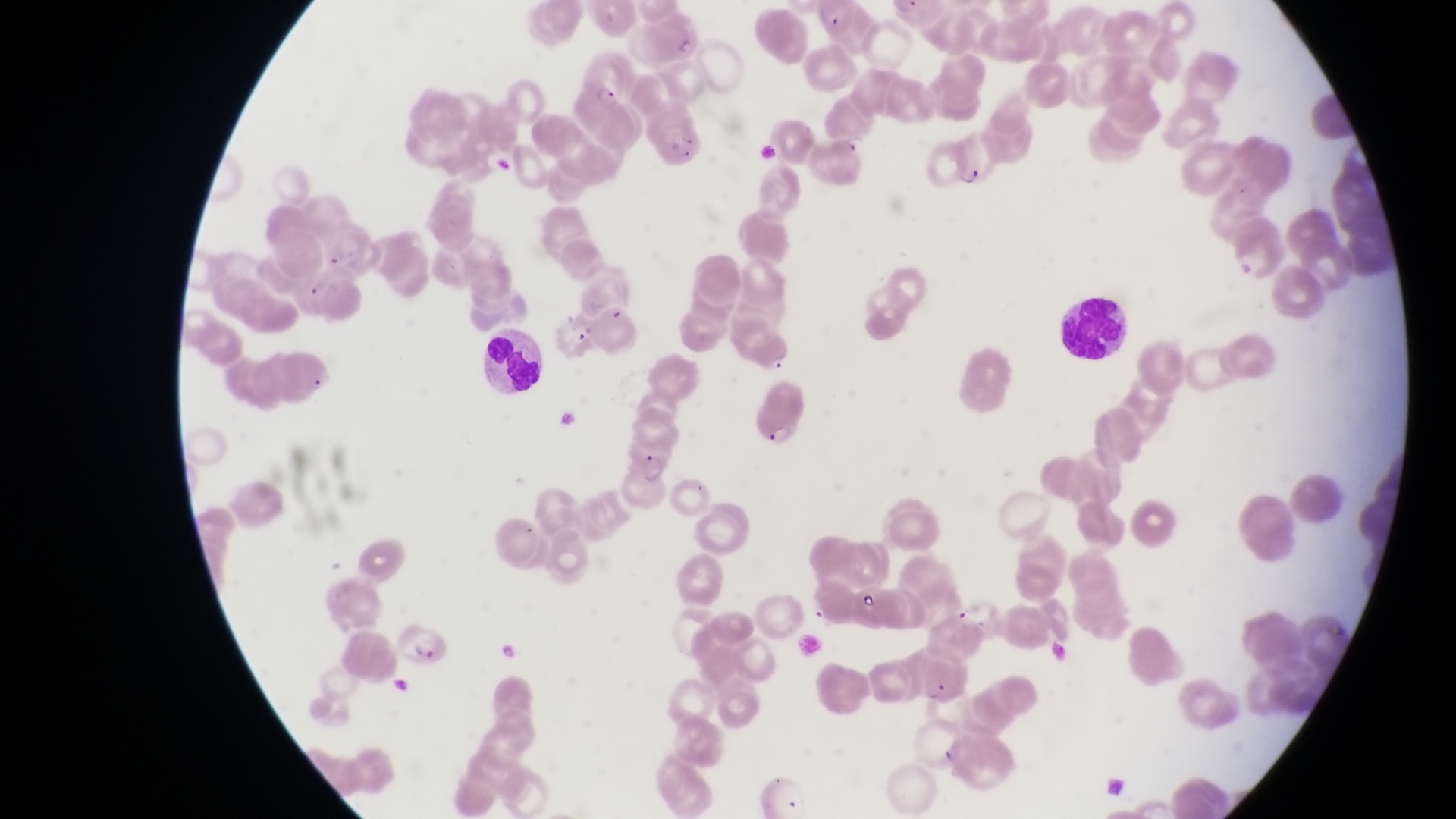
Approximate bounding boxes as {left, top, right, bottom} in pixels.
Summary:
  - Trophozoite locations: {838, 127, 872, 153}, {957, 165, 987, 192}
  - Parasitised red blood cell locations: {570, 55, 636, 114}, {642, 112, 711, 167}, {394, 616, 452, 674}
  - Artifact (platelet-like body, stain precipitate, or debris) locations: {486, 149, 513, 181}, {858, 582, 882, 616}
  - Leukocyte locations: {1065, 290, 1129, 364}, {479, 330, 543, 396}
  - Image size: 1456×819 pixels
  - Magnification: 1000x
  - Preparation: thin blood smear
  - Field of view: single
  - Capture: smartphone photograph through the eyepiece of an Olympus CX-23 microscope
  - Country: Uganda